Locate and identify every blood parasite.
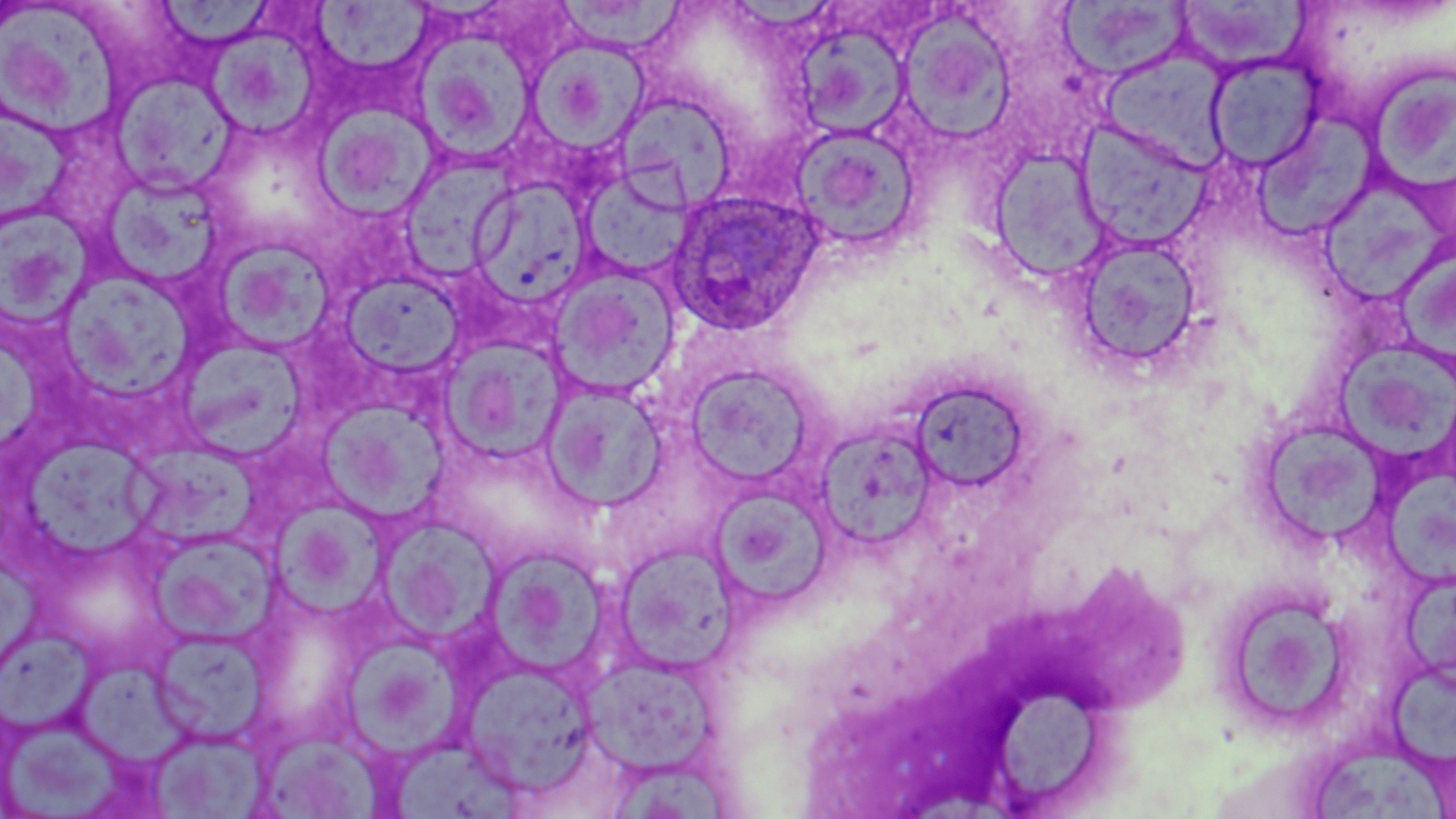
Approximate bounding boxes as (x1, y1, x2, y2) in pixels.
Plasmodium ovale-infected red blood cells: (666, 189, 825, 335).
No Plasmodium falciparum, Plasmodium malariae, Plasmodium vivax, Babesia divergens, or Trypanosoma brucei observed.

Uninfected red blood cell locations: (558, 0, 694, 54), (153, 1, 276, 50), (1057, 2, 1192, 80), (1172, 2, 1311, 73), (309, 3, 435, 76), (0, 9, 127, 136), (897, 11, 1017, 144), (793, 19, 913, 139), (204, 26, 320, 138), (417, 37, 539, 163), (533, 39, 648, 149), (1099, 47, 1234, 171), (1205, 53, 1325, 172), (1367, 66, 1456, 194), (110, 72, 241, 196), (613, 93, 739, 213), (314, 105, 441, 218), (1259, 112, 1382, 243), (0, 113, 80, 226), (1075, 119, 1211, 252), (787, 123, 923, 253), (988, 146, 1111, 283), (398, 153, 518, 281), (579, 166, 695, 281), (102, 169, 234, 289), (467, 177, 594, 309), (1321, 183, 1451, 306), (0, 204, 98, 328), (1069, 233, 1204, 374), (212, 238, 338, 354), (1394, 246, 1456, 361), (548, 264, 681, 399), (339, 272, 464, 378), (70, 278, 196, 401), (442, 338, 570, 463), (184, 341, 314, 458), (1339, 347, 1456, 460), (684, 363, 817, 487), (909, 378, 1032, 494), (541, 379, 669, 512), (326, 405, 456, 521), (813, 423, 939, 549), (1268, 424, 1388, 546), (21, 438, 169, 561), (123, 447, 268, 548), (1381, 470, 1456, 586), (709, 494, 834, 607), (275, 498, 387, 627), (378, 517, 500, 643), (148, 528, 281, 644), (611, 541, 739, 673), (481, 544, 613, 680), (1402, 577, 1456, 690), (1216, 585, 1352, 731), (0, 627, 95, 738), (150, 628, 272, 747), (344, 641, 467, 762), (579, 653, 724, 776), (1390, 655, 1456, 774), (78, 659, 212, 772), (461, 660, 598, 792), (995, 691, 1105, 804), (2, 712, 138, 817), (149, 728, 269, 818), (264, 734, 387, 819), (390, 735, 525, 818), (1312, 746, 1448, 819), (609, 763, 729, 819). Slide-level diagnosis: Plasmodium ovale. One field of a larger specimen. Optical microscopy. Image is 1456×819 pixels. Thin blood smear. 1000x magnification. May-Grünwald-Giemsa-stained preparation.